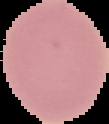
Summary:
  - Result: no Plasmodium parasites detected
  - Image type: segmented cell region with the area outside set to black
  - Preparation: thin blood film
  - Image size: 109×124 pixels